Identify the parasite.
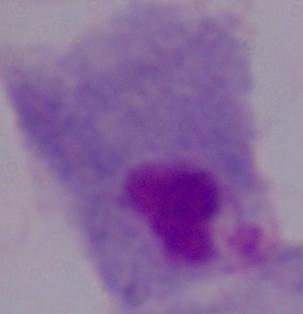
A trichomonad.

{
  "magnification": "1000x",
  "modality": "photomicrograph"
}